Assess for malaria.
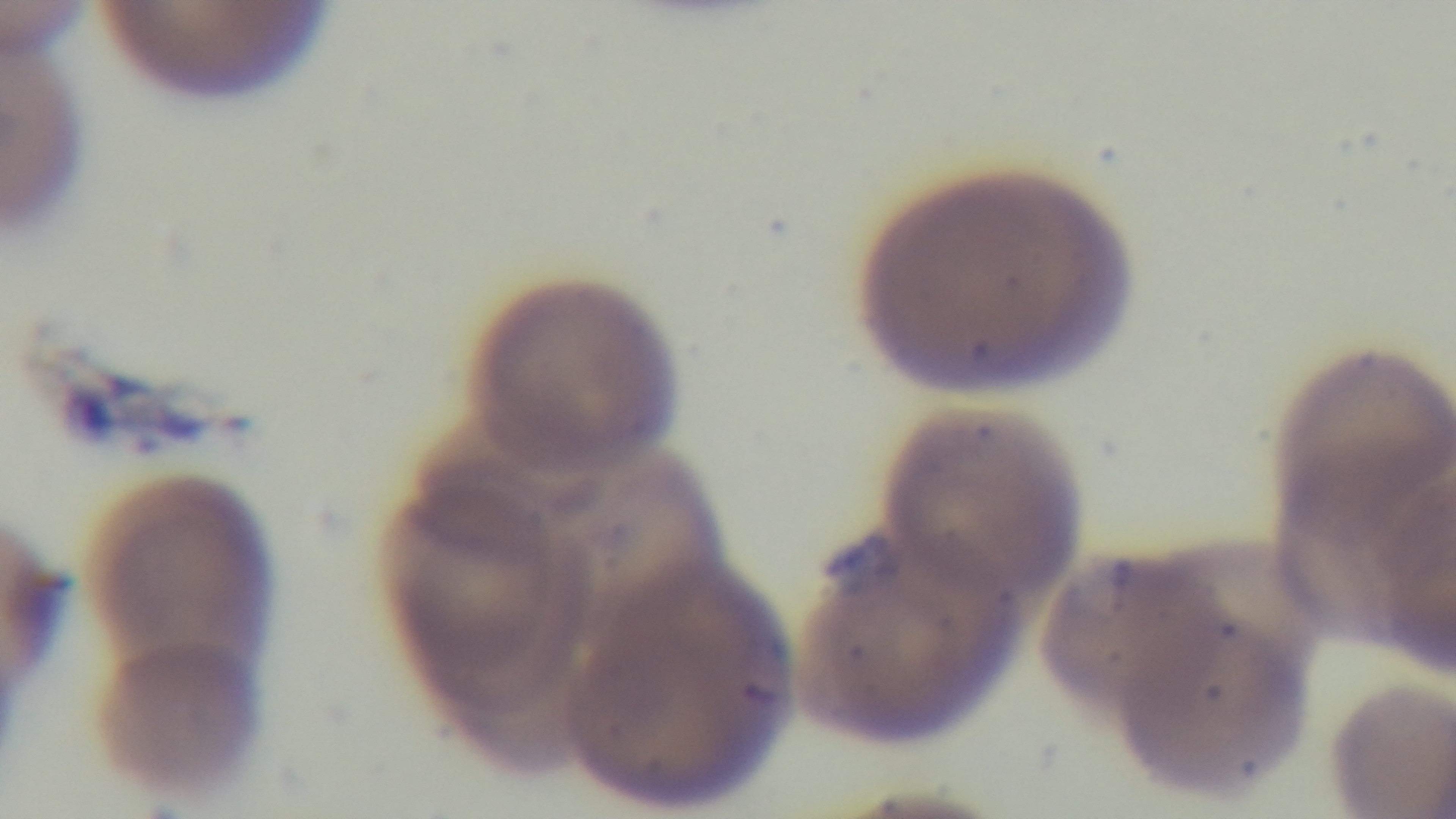

Positive.

modality = light microscopy
capture = mounted 4K digital camera
stain = Giemsa
preparation = thin
field of view = single
objective = 100x oil immersion